Report the malaria status of this cell.
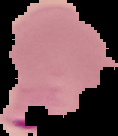
It is parasitized.

image type = cell region segmented out of the field of view; surrounding area masked to black
image size = 118×136 pixels
preparation = thin blood smear